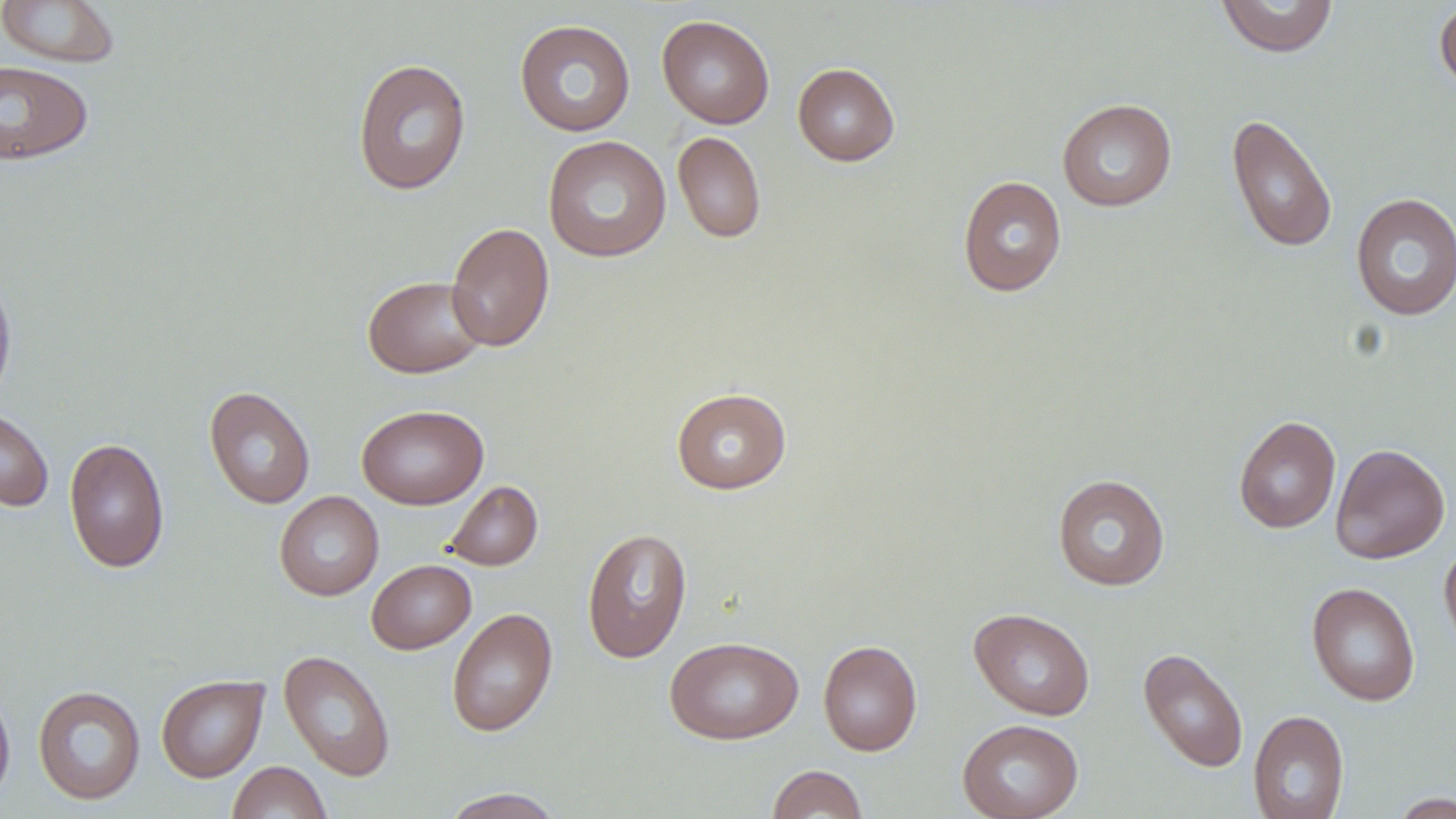
slide-level diagnosis = negative for blood parasites
magnification = 1000x
preparation = thin blood smear
uninfected red blood cell locations = approximate bounding boxes as (x1,y1)-(x2,y2) corner pairs in pixels: (0,0)-(122,68), (1215,1)-(1340,58), (1434,1)-(1456,94), (657,15)-(774,128), (514,19)-(636,137), (352,58)-(472,195), (0,60)-(94,166), (792,62)-(900,166), (1056,98)-(1177,212), (1226,113)-(1338,254), (672,131)-(766,244), (543,135)-(672,262), (957,175)-(1067,297), (1350,193)-(1456,321), (445,221)-(555,352), (0,268)-(17,408), (362,275)-(488,378), (204,386)-(315,509), (671,387)-(792,494), (357,404)-(488,510), (0,406)-(55,512), (1233,415)-(1341,534), (64,437)-(170,574), (1330,443)-(1450,564), (1052,474)-(1170,592), (445,481)-(543,571), (274,490)-(384,601), (582,527)-(692,663), (1439,540)-(1456,653), (366,559)-(476,654), (1306,582)-(1421,707), (446,607)-(557,738), (969,608)-(1095,720), (664,635)-(803,744), (818,640)-(922,756), (1137,647)-(1249,773), (278,649)-(396,782), (156,674)-(269,782), (0,684)-(15,807), (32,685)-(146,805), (1248,710)-(1350,819), (957,719)-(1083,819), (227,761)-(332,819), (767,764)-(868,819), (438,787)-(567,818), (1386,792)-(1455,818)
image size = 1456×819 pixels
field of view = single
modality = light microscopy
stain = May-Grünwald-Giemsa